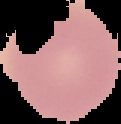

image_type: cell region segmented out of the field of view; surrounding area masked to black
malaria_status: uninfected
preparation: thin blood smear
image_size: 121×124 pixels